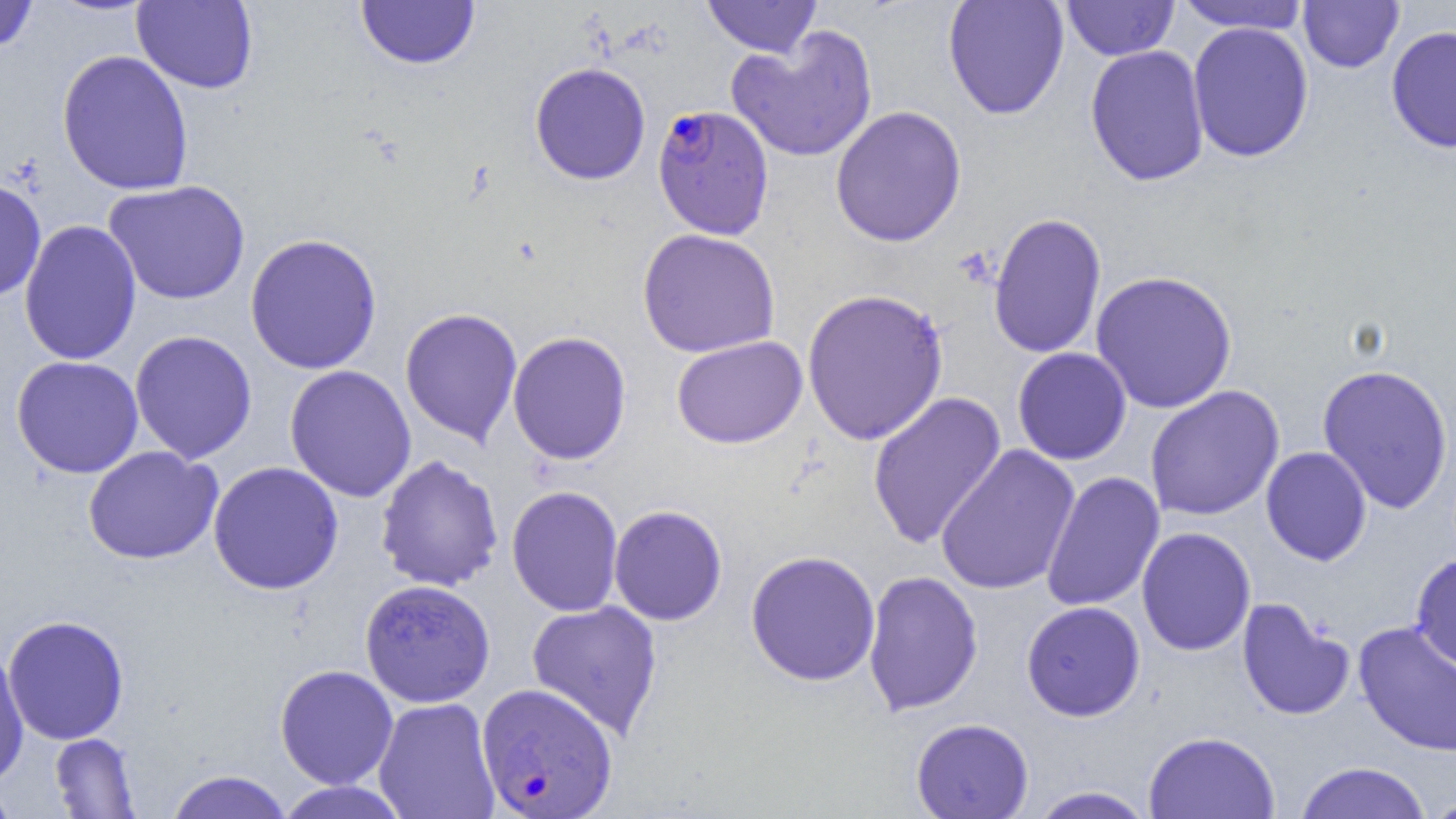

Approximate bounding boxes as named x1/y1/x2/y2 corners in pixels. Plasmodium falciparum-infected red blood cell locations: (x1=651, y1=104, x2=774, y2=240), (x1=476, y1=682, x2=618, y2=818). Uninfected red blood cell locations: (x1=0, y1=0, x2=38, y2=55), (x1=702, y1=0, x2=822, y2=58), (x1=942, y1=0, x2=1069, y2=120), (x1=1061, y1=0, x2=1179, y2=61), (x1=132, y1=1, x2=259, y2=94), (x1=356, y1=1, x2=480, y2=70), (x1=1174, y1=1, x2=1312, y2=34), (x1=1298, y1=1, x2=1405, y2=74), (x1=1187, y1=22, x2=1314, y2=163), (x1=726, y1=25, x2=879, y2=163), (x1=1385, y1=25, x2=1456, y2=153), (x1=1084, y1=45, x2=1211, y2=187), (x1=56, y1=50, x2=194, y2=196), (x1=529, y1=62, x2=651, y2=185), (x1=830, y1=105, x2=967, y2=248), (x1=0, y1=176, x2=47, y2=303), (x1=103, y1=180, x2=251, y2=306), (x1=987, y1=212, x2=1107, y2=359), (x1=18, y1=219, x2=142, y2=366), (x1=637, y1=228, x2=780, y2=358), (x1=244, y1=232, x2=382, y2=375), (x1=1090, y1=270, x2=1238, y2=414), (x1=801, y1=288, x2=949, y2=446), (x1=399, y1=307, x2=523, y2=447), (x1=129, y1=330, x2=258, y2=464), (x1=506, y1=330, x2=632, y2=466), (x1=671, y1=335, x2=808, y2=449), (x1=1012, y1=347, x2=1132, y2=465), (x1=10, y1=355, x2=144, y2=479), (x1=1316, y1=363, x2=1455, y2=515), (x1=283, y1=364, x2=417, y2=502), (x1=1145, y1=385, x2=1285, y2=521), (x1=867, y1=391, x2=1007, y2=549), (x1=935, y1=444, x2=1081, y2=596), (x1=83, y1=446, x2=223, y2=565), (x1=1260, y1=446, x2=1372, y2=566), (x1=375, y1=454, x2=504, y2=592), (x1=207, y1=461, x2=344, y2=595), (x1=1041, y1=470, x2=1165, y2=612), (x1=506, y1=485, x2=624, y2=617), (x1=608, y1=505, x2=728, y2=626), (x1=1136, y1=526, x2=1256, y2=656), (x1=745, y1=550, x2=881, y2=687), (x1=1410, y1=552, x2=1456, y2=672), (x1=862, y1=569, x2=984, y2=717), (x1=359, y1=578, x2=496, y2=708), (x1=1236, y1=598, x2=1356, y2=721), (x1=526, y1=600, x2=664, y2=740), (x1=1021, y1=601, x2=1145, y2=721), (x1=2, y1=614, x2=130, y2=745), (x1=1352, y1=621, x2=1456, y2=757), (x1=0, y1=644, x2=30, y2=788), (x1=275, y1=664, x2=398, y2=789), (x1=373, y1=697, x2=500, y2=819), (x1=911, y1=718, x2=1034, y2=818), (x1=1143, y1=730, x2=1280, y2=819), (x1=49, y1=732, x2=141, y2=817), (x1=1294, y1=761, x2=1432, y2=818), (x1=164, y1=769, x2=293, y2=819), (x1=275, y1=781, x2=409, y2=819), (x1=0, y1=783, x2=19, y2=819), (x1=1026, y1=786, x2=1157, y2=818), (x1=1422, y1=794, x2=1456, y2=818). Slide-level diagnosis: Plasmodium falciparum. Single field of view. Thin blood film. Image is 1456×819 pixels. Light microscopy. Captured at 1000x magnification.